Point out each Plasmodium parasite.
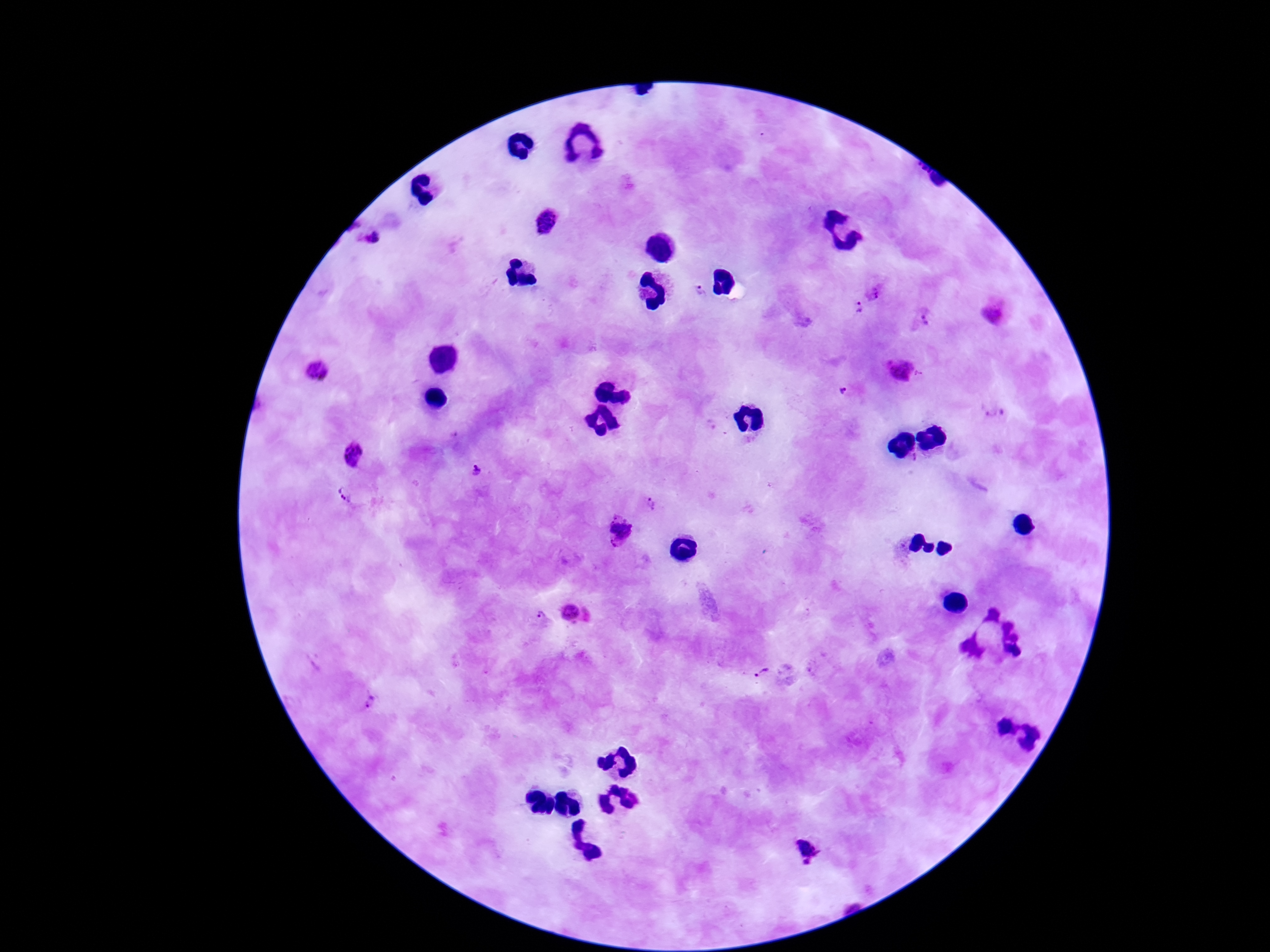

Approximate centers as [x, y] in pixels.
Plasmodium parasites: [547, 222], [370, 237], [702, 291], [874, 291], [859, 306], [994, 313], [921, 319], [318, 371], [901, 373], [844, 392], [993, 411], [354, 455], [916, 458], [476, 471], [348, 492], [653, 504], [620, 532], [575, 615], [541, 616], [762, 672], [366, 698], [807, 850].

{
  "field_of_view": "one from this slide",
  "capture": "smartphone camera through the microscope eyepiece",
  "patient_malaria_status": "positive",
  "stain": "Giemsa",
  "magnification": "100x",
  "image_size": "1270×952 pixels",
  "preparation": "thick peripheral-blood smear"
}